State which parasite is depicted.
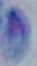

Toxoplasma gondii.

{
  "modality": "photomicrograph",
  "magnification": "1000x"
}